Report the malaria status of this cell.
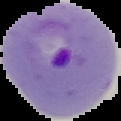
Parasitized.

From a thin blood film. Image is 121×121 pixels. The area outside the segmented cell region is set to black.